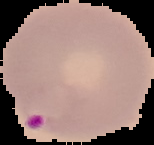
The area outside the segmented cell region is set to black. Malaria status: parasitized. From a thin blood smear. Image is 154×145 pixels.